Name the blood parasite species.
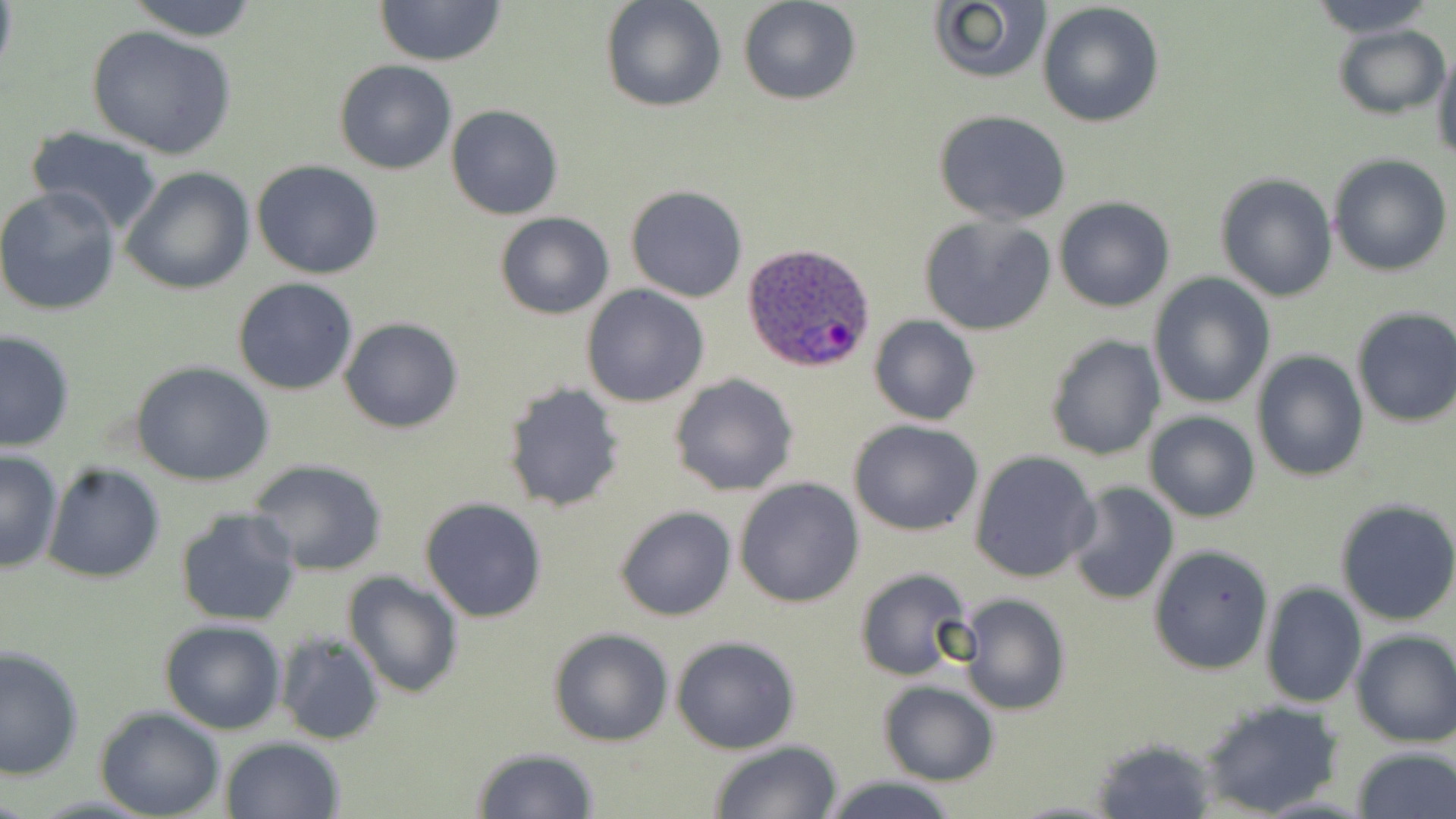

Plasmodium ovale.

Approximate bounding boxes as (x1, y1, x2, y2) in pixels. Uninfected red blood cell locations: (122, 0, 261, 41), (374, 0, 507, 66), (599, 0, 727, 114), (738, 0, 861, 106), (1308, 0, 1439, 37), (925, 1, 1053, 87), (1036, 2, 1166, 130), (1332, 22, 1451, 120), (87, 27, 236, 161), (1431, 40, 1456, 168), (334, 60, 456, 174), (445, 104, 563, 220), (932, 111, 1073, 226), (23, 128, 165, 236), (1328, 154, 1452, 277), (252, 159, 384, 280), (120, 166, 255, 295), (1215, 172, 1338, 301), (0, 185, 122, 316), (626, 185, 748, 302), (1053, 197, 1176, 313), (496, 212, 615, 319), (917, 214, 1056, 336), (1148, 274, 1275, 409), (232, 276, 359, 396), (580, 285, 710, 408), (1349, 307, 1456, 429), (868, 315, 980, 425), (339, 316, 464, 433), (1, 327, 75, 453), (1045, 333, 1164, 461), (1251, 350, 1368, 482), (132, 363, 276, 485), (668, 374, 799, 496), (502, 381, 626, 511), (1144, 410, 1260, 523), (848, 418, 984, 537), (0, 451, 63, 573), (969, 451, 1100, 582), (246, 460, 388, 576), (43, 462, 165, 584), (734, 477, 864, 608), (1064, 480, 1180, 607), (419, 496, 549, 623), (1334, 498, 1456, 626), (613, 506, 737, 622), (175, 507, 303, 628), (1147, 544, 1274, 675), (852, 565, 974, 682), (342, 571, 464, 698), (1259, 581, 1367, 709), (955, 593, 1070, 716), (159, 619, 287, 735), (548, 627, 675, 747), (1349, 629, 1456, 747), (274, 630, 387, 746), (672, 635, 800, 753), (0, 645, 82, 780), (878, 681, 998, 785), (1197, 699, 1346, 817), (95, 707, 224, 819), (1090, 735, 1220, 817), (219, 736, 346, 819), (706, 741, 844, 819), (1350, 744, 1455, 819), (470, 746, 600, 818), (817, 774, 965, 819). Plasmodium ovale-infected red blood cell locations: (741, 244, 876, 373). Image is 1456×819 pixels. Captured at 1000x magnification. Single field of view. Thin blood smear. May-Grünwald-Giemsa-stained preparation. Light microscopy.